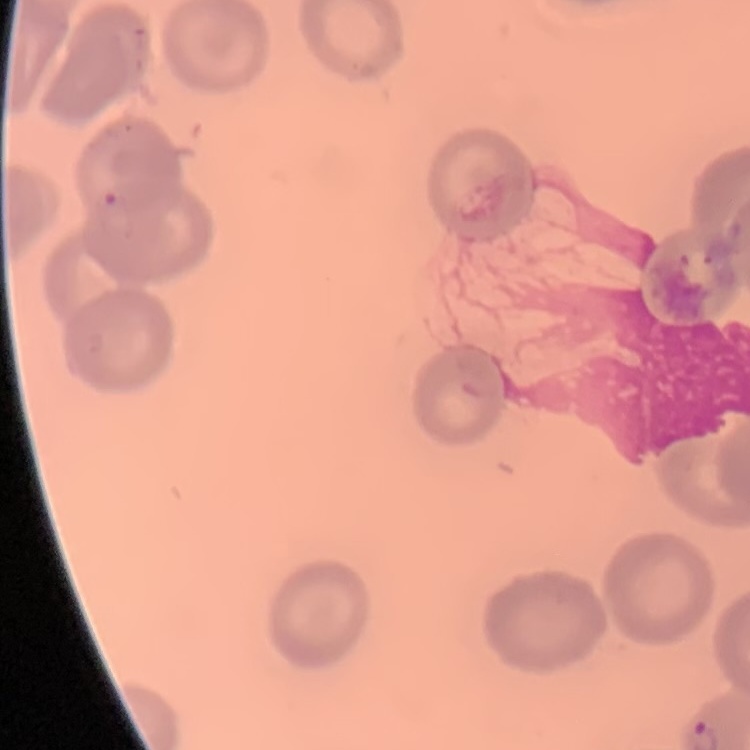 The erythrocytes exhibit no rouleaux formation. Square crop of a larger photomicrograph. Stained with either Field's or Giemsa. Thin blood smear.